Report the malaria status of this cell.
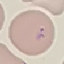
It is parasitized.

{
  "stain": "Giemsa",
  "preparation": "thin smear",
  "image_type": "cell patch, automatically extracted from a larger field of view and resized to 64 × 64 pixels",
  "capture": "smartphone camera at the microscope eyepiece"
}